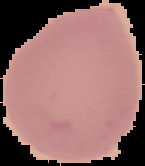

{
  "preparation": "thin blood smear",
  "image_size": "145×166 pixels",
  "image_type": "cell region segmented out of the field of view; surrounding area masked to black",
  "malaria_status": "uninfected"
}